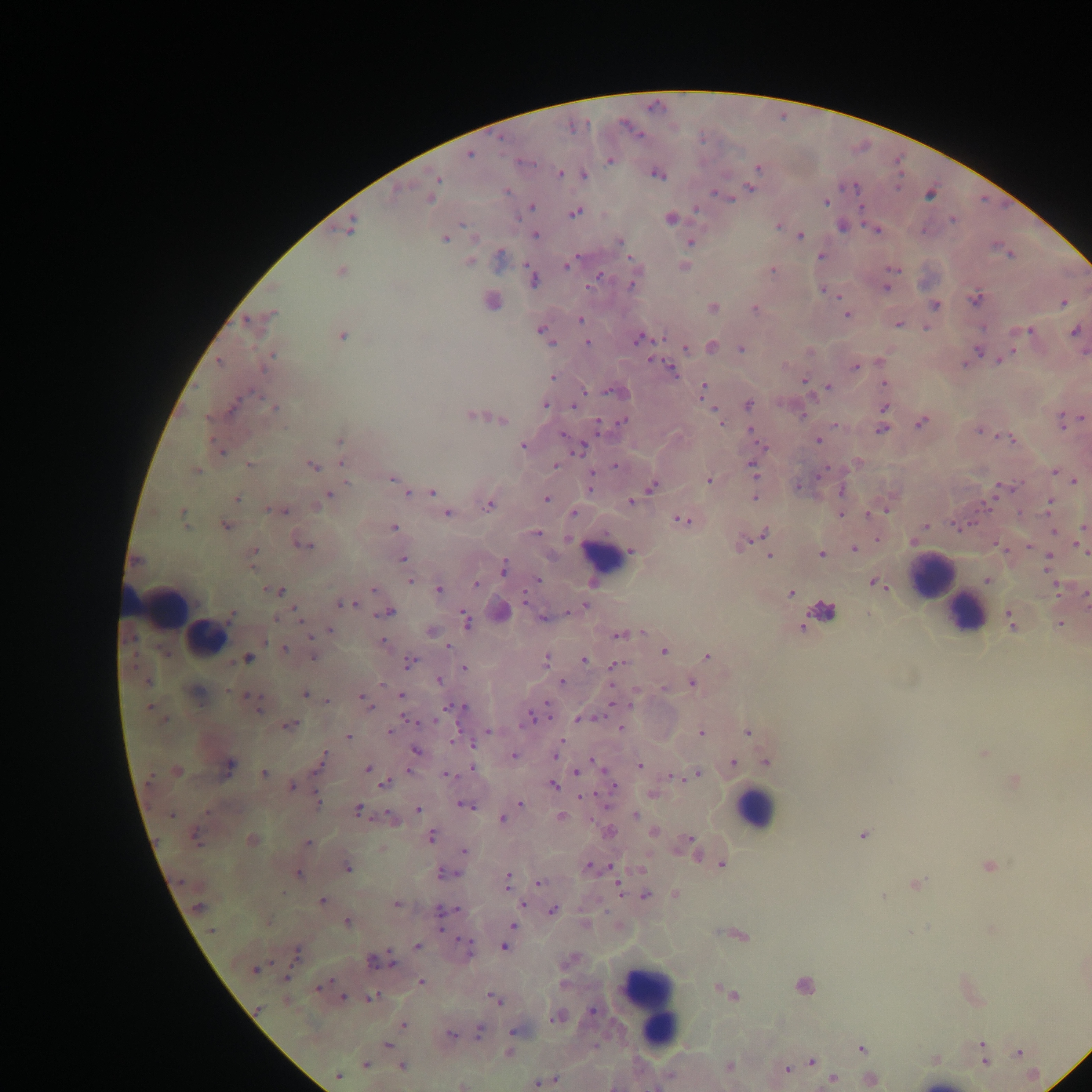 Approximate centers as [x, y] in pixels. Leukocyte locations: [595, 554], [930, 576], [160, 602], [965, 612], [206, 637], [757, 808], [649, 1002], [941, 1083]. Malaria parasite locations: [469, 155], [610, 161], [523, 162], [757, 169], [560, 174], [584, 174], [658, 174], [436, 180], [749, 187], [853, 188], [506, 191], [397, 192], [930, 195], [720, 196], [431, 198], [826, 203], [532, 207], [696, 209], [574, 213], [670, 219], [953, 219], [350, 226], [777, 226], [842, 226], [877, 230], [535, 235], [800, 236], [445, 238], [620, 242], [691, 243], [500, 256], [821, 256], [469, 262], [567, 265], [685, 266], [894, 269], [340, 271], [772, 271], [600, 277], [533, 279], [633, 283], [886, 288], [824, 290], [976, 299], [491, 302], [1064, 303], [935, 305], [712, 307], [754, 309], [272, 314], [847, 315], [580, 320], [247, 322], [898, 325], [926, 328], [1029, 329], [542, 332], [1075, 332], [342, 336], [639, 339], [587, 342], [712, 347], [741, 348], [685, 349], [978, 351], [1084, 351], [269, 358], [880, 361], [999, 361], [219, 362], [854, 367], [671, 370], [551, 377], [804, 381], [884, 383], [828, 387], [703, 391], [614, 392], [545, 405], [574, 405], [748, 405], [885, 407], [274, 408], [801, 415], [472, 416], [1081, 417], [501, 419], [623, 421], [720, 421], [1062, 421], [921, 423], [600, 425], [881, 430], [979, 430], [750, 431], [565, 436], [1008, 438], [339, 441], [818, 441], [524, 446], [580, 446], [220, 451], [341, 463], [249, 465], [312, 465], [556, 465], [616, 466], [753, 470], [196, 471], [1056, 473], [592, 475], [392, 478], [710, 480], [1074, 481], [652, 487], [799, 487], [842, 490], [433, 492], [408, 493], [329, 496], [754, 496], [236, 499], [547, 499], [631, 503], [318, 504], [1049, 504], [489, 506], [285, 512], [182, 513], [574, 513], [840, 513], [874, 513], [448, 514], [682, 519], [225, 526], [926, 526], [393, 527], [1085, 527], [1054, 531], [536, 533], [765, 534], [304, 544], [740, 545], [1029, 546], [1001, 547], [854, 548], [1082, 549], [254, 551], [631, 552], [822, 554], [769, 555], [1048, 558], [402, 559], [137, 561], [252, 564], [504, 569], [410, 580], [536, 580], [987, 580], [874, 583], [476, 584], [1057, 585], [374, 589], [439, 589], [269, 590], [278, 591], [791, 593], [1085, 595], [526, 598], [341, 603], [353, 605], [584, 607], [388, 612], [297, 613], [232, 614], [542, 618], [301, 620], [465, 620], [1011, 621], [1060, 625], [802, 628], [330, 630], [431, 632], [642, 632], [621, 635], [310, 636], [384, 643], [447, 646], [285, 649], [664, 651], [708, 656], [314, 657], [248, 658], [546, 660], [584, 660], [409, 663], [617, 664], [464, 668], [439, 680], [148, 681], [561, 681], [692, 683], [382, 684], [663, 689], [197, 693], [304, 695], [401, 695], [252, 698], [363, 698], [326, 700], [365, 703], [257, 704], [459, 707], [149, 708], [450, 708], [584, 718], [531, 719], [164, 720], [410, 721], [291, 725], [620, 729], [390, 731], [489, 731], [701, 732], [747, 732], [348, 737], [457, 740], [469, 744], [416, 751], [984, 753], [557, 754], [514, 756], [322, 757], [767, 762], [733, 763], [319, 764], [640, 765], [228, 766], [473, 767], [368, 769], [177, 771], [577, 772], [264, 773], [697, 774], [447, 775], [676, 777], [1014, 781], [385, 784], [553, 785], [613, 786], [292, 787], [653, 794], [582, 796], [318, 800], [520, 804], [464, 805], [358, 809], [418, 810], [636, 814], [171, 815], [391, 816], [562, 817], [502, 819], [653, 832], [863, 834], [432, 836], [196, 837], [252, 839], [308, 843], [690, 843], [464, 852], [722, 864], [989, 866], [347, 867], [590, 867], [298, 873], [447, 873], [508, 879], [540, 882], [916, 883], [619, 889], [282, 893], [675, 894], [646, 895], [883, 897], [322, 901], [397, 903], [522, 904], [198, 907], [553, 910], [444, 911], [347, 922], [513, 925], [441, 929], [212, 931], [741, 935], [466, 942], [416, 946], [505, 948], [297, 953], [376, 961], [392, 962], [255, 969], [286, 977], [421, 982], [804, 986], [318, 988], [723, 990], [732, 995], [343, 998], [372, 998], [495, 1000], [258, 1009], [593, 1011], [557, 1017], [403, 1025], [479, 1032], [513, 1032], [451, 1034], [387, 1044], [982, 1045], [862, 1049], [1019, 1052], [509, 1053], [984, 1060], [812, 1061], [366, 1064], [401, 1066], [729, 1067], [786, 1069], [339, 1075], [833, 1079], [871, 1079], [553, 1080], [544, 1082], [537, 1083]. Photographed through a microscope with a mobile-phone camera. Thick blood smear. Collected in Ghana. Image is 1092×1092 pixels. One field of view.